State the blood parasite species.
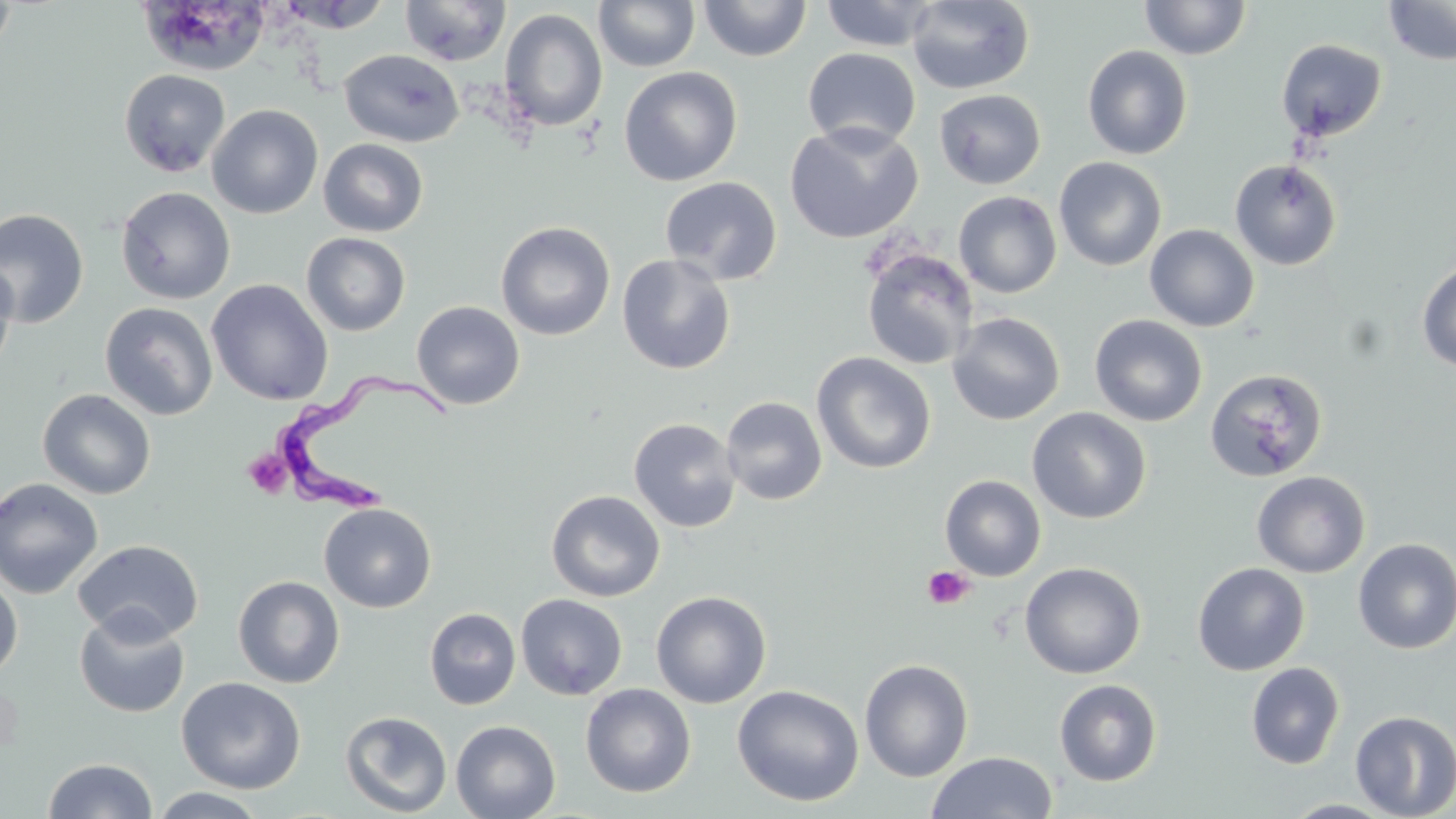

Trypanosoma brucei.

{
  "preparation": "thin blood smear",
  "magnification": "1000x",
  "field_of_view": "one of a larger specimen",
  "uninfected_red_blood_cell_locations": "approximate bounding boxes as (x1,y1)-(x2,y2) corner pairs in pixels: (139,0)-(270,76), (274,0)-(393,33), (399,0)-(511,67), (593,0)-(701,72), (698,0)-(812,62), (906,0)-(1035,95), (1140,0)-(1252,60), (0,1)-(18,57), (818,1)-(942,51), (1384,1)-(1456,66), (499,8)-(608,132), (1276,38)-(1387,142), (1081,45)-(1193,160), (802,48)-(921,150), (339,49)-(464,148), (618,66)-(742,187), (119,69)-(230,177), (933,89)-(1046,190), (207,104)-(323,219), (784,121)-(924,244), (318,138)-(429,237), (1053,156)-(1167,271), (1229,158)-(1343,271), (659,176)-(783,285), (115,186)-(236,304), (953,191)-(1062,298), (0,208)-(89,329), (496,221)-(615,341), (1144,223)-(1259,332), (301,232)-(411,336), (861,247)-(978,371), (617,253)-(737,375), (0,258)-(17,376), (1416,261)-(1456,373), (206,278)-(333,406), (99,301)-(218,420), (412,301)-(525,410), (947,312)-(1065,426), (1089,314)-(1208,427), (812,351)-(935,474), (1204,368)-(1329,483), (37,389)-(156,500), (721,396)-(827,505), (1027,407)-(1152,524), (628,417)-(742,533), (1251,470)-(1371,578), (939,475)-(1046,581), (0,477)-(104,600), (546,490)-(665,602), (318,502)-(437,613), (1353,537)-(1456,654), (72,539)-(204,644), (1019,561)-(1146,679), (1192,562)-(1310,676), (0,575)-(23,682), (233,576)-(345,688), (651,590)-(772,708), (516,593)-(628,700), (74,608)-(191,718), (424,608)-(521,710), (858,658)-(974,782), (1245,662)-(1345,769), (175,676)-(306,794), (1054,679)-(1162,786), (580,683)-(696,798), (731,684)-(865,807), (340,710)-(453,817), (1350,710)-(1456,819), (451,719)-(561,819), (925,751)-(1058,819), (43,757)-(157,818), (147,787)-(269,818), (1280,799)-(1399,818)",
  "platelet_locations": "approximate bounding boxes as (x1,y1)-(x2,y2) corner pairs in pixels: (242,449)-(292,498), (921,566)-(974,610)",
  "trypanosoma_brucei_locations": "approximate bounding boxes as (x1,y1)-(x2,y2) corner pairs in pixels: (271,369)-(457,515)",
  "stain": "May-Grünwald-Giemsa",
  "image_size": "1456×819 pixels",
  "modality": "optical microscopy"
}